Classify this cell by malaria status.
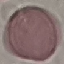
Uninfected.

Automatically extracted cell patch, resized to 64 × 64 pixels. Thin smear of blood. Giemsa-stained preparation. Photographed with a smartphone camera at the microscope eyepiece.